Outline each blood parasite and name the species.
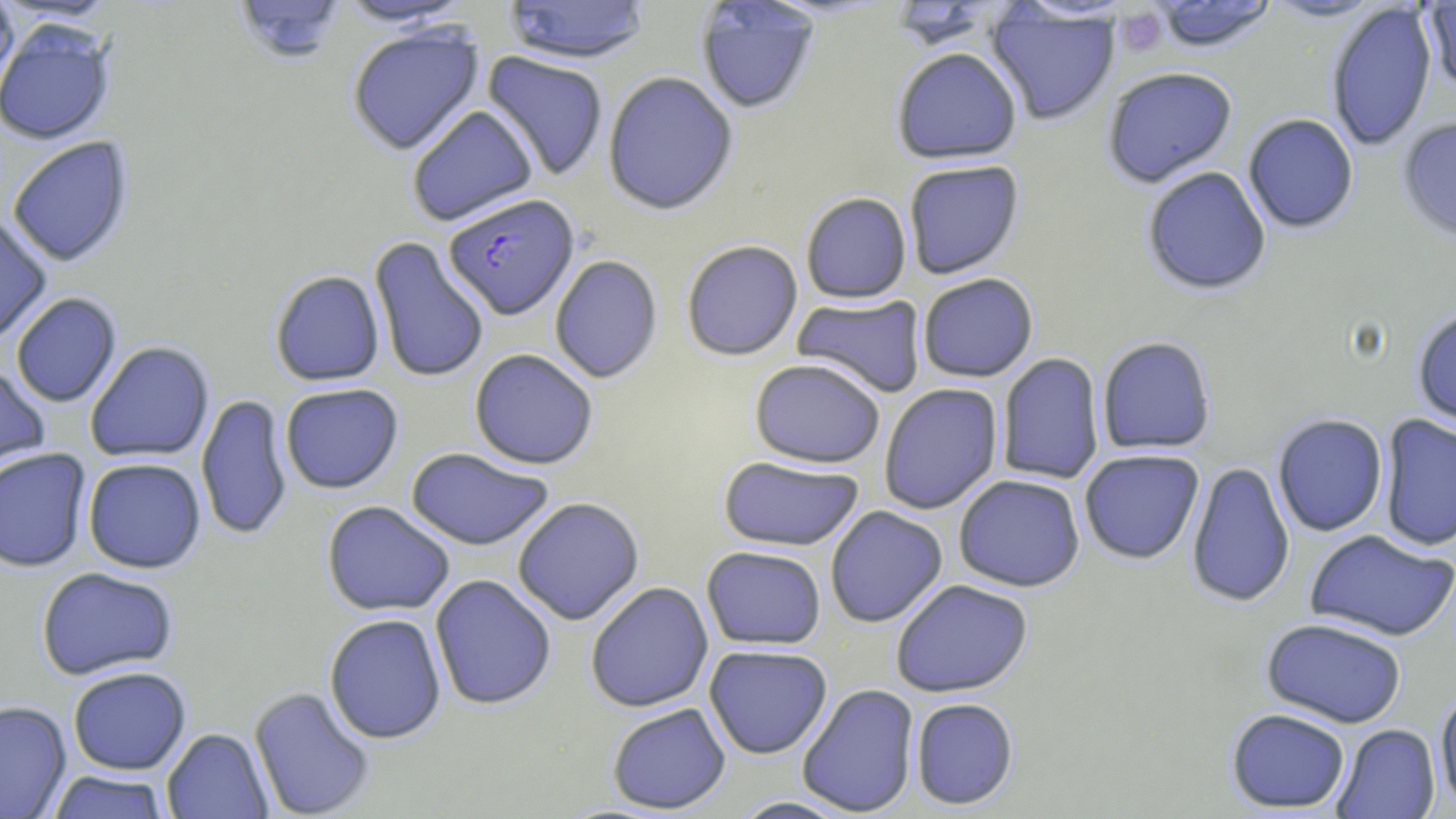
Approximate bounding boxes as (x1, y1, x2, y2) in pixels.
Plasmodium falciparum-infected red blood cells: (444, 193, 579, 320).
No Plasmodium ovale, Plasmodium malariae, Plasmodium vivax, Babesia divergens, or Trypanosoma brucei observed.

Summary:
  - Platelet locations: (1115, 7, 1167, 56)
  - Uninfected red blood cell locations: (231, 0, 348, 65), (333, 0, 475, 28), (502, 0, 652, 65), (1149, 0, 1279, 53), (1261, 0, 1388, 23), (695, 1, 820, 115), (0, 2, 20, 97), (886, 2, 1007, 52), (1423, 2, 1456, 92), (1326, 3, 1438, 152), (985, 6, 1120, 126), (0, 21, 116, 146), (346, 23, 485, 155), (891, 47, 1023, 165), (481, 51, 609, 182), (1101, 67, 1238, 188), (602, 71, 739, 215), (407, 104, 538, 226), (1243, 113, 1359, 234), (1397, 116, 1456, 244), (6, 136, 135, 267), (903, 160, 1025, 279), (1141, 166, 1272, 295), (800, 192, 912, 304), (0, 212, 52, 347), (369, 235, 490, 384), (681, 239, 803, 361), (550, 254, 663, 384), (269, 269, 385, 386), (917, 273, 1039, 382), (11, 292, 122, 408), (792, 294, 927, 398), (1411, 306, 1456, 429), (1097, 335, 1217, 454), (85, 341, 215, 463), (469, 348, 599, 470), (996, 353, 1105, 485), (749, 358, 885, 468), (0, 362, 51, 483), (280, 383, 404, 494), (879, 383, 1003, 515), (197, 394, 292, 541), (1272, 413, 1388, 537), (1378, 415, 1456, 552), (0, 447, 92, 572), (405, 447, 555, 550), (1079, 449, 1205, 564), (718, 456, 865, 551), (82, 457, 206, 573), (1186, 461, 1296, 609), (953, 474, 1085, 592), (512, 496, 645, 625), (321, 501, 455, 616), (825, 506, 948, 628), (1304, 529, 1456, 643), (702, 545, 826, 650), (36, 566, 178, 681), (429, 574, 556, 711), (891, 579, 1034, 698), (585, 582, 714, 712), (324, 613, 447, 744), (1261, 617, 1408, 728), (704, 645, 833, 759), (68, 666, 191, 775), (797, 683, 920, 817), (249, 685, 376, 819), (1434, 687, 1456, 811), (910, 698, 1019, 810), (0, 700, 72, 818), (606, 703, 731, 814), (1226, 707, 1351, 813), (1332, 724, 1440, 818), (162, 728, 273, 818), (46, 770, 171, 818), (729, 796, 855, 818)
  - Slide-level diagnosis: Plasmodium falciparum
  - Magnification: 1000x
  - Stain: May-Grünwald-Giemsa
  - Preparation: thin blood smear
  - Modality: optical microscopy
  - Image size: 1456×819 pixels
  - Field of view: one of a larger specimen